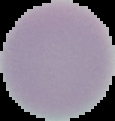 Result: no Plasmodium parasites detected. Image is 115×121 pixels. From a thin blood film. The area outside the segmented cell region is set to black.